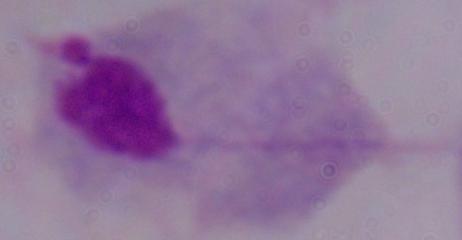

{
  "modality": "photomicrograph",
  "magnification": "1000x",
  "identification": "trichomonad"
}